Assess this cell for malaria.
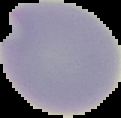
Uninfected.

Summary:
  - Image type: cell region segmented out of the field of view; surrounding area masked to black
  - Preparation: thin blood smear
  - Image size: 121×118 pixels